Locate every leukocyte (white blood cell).
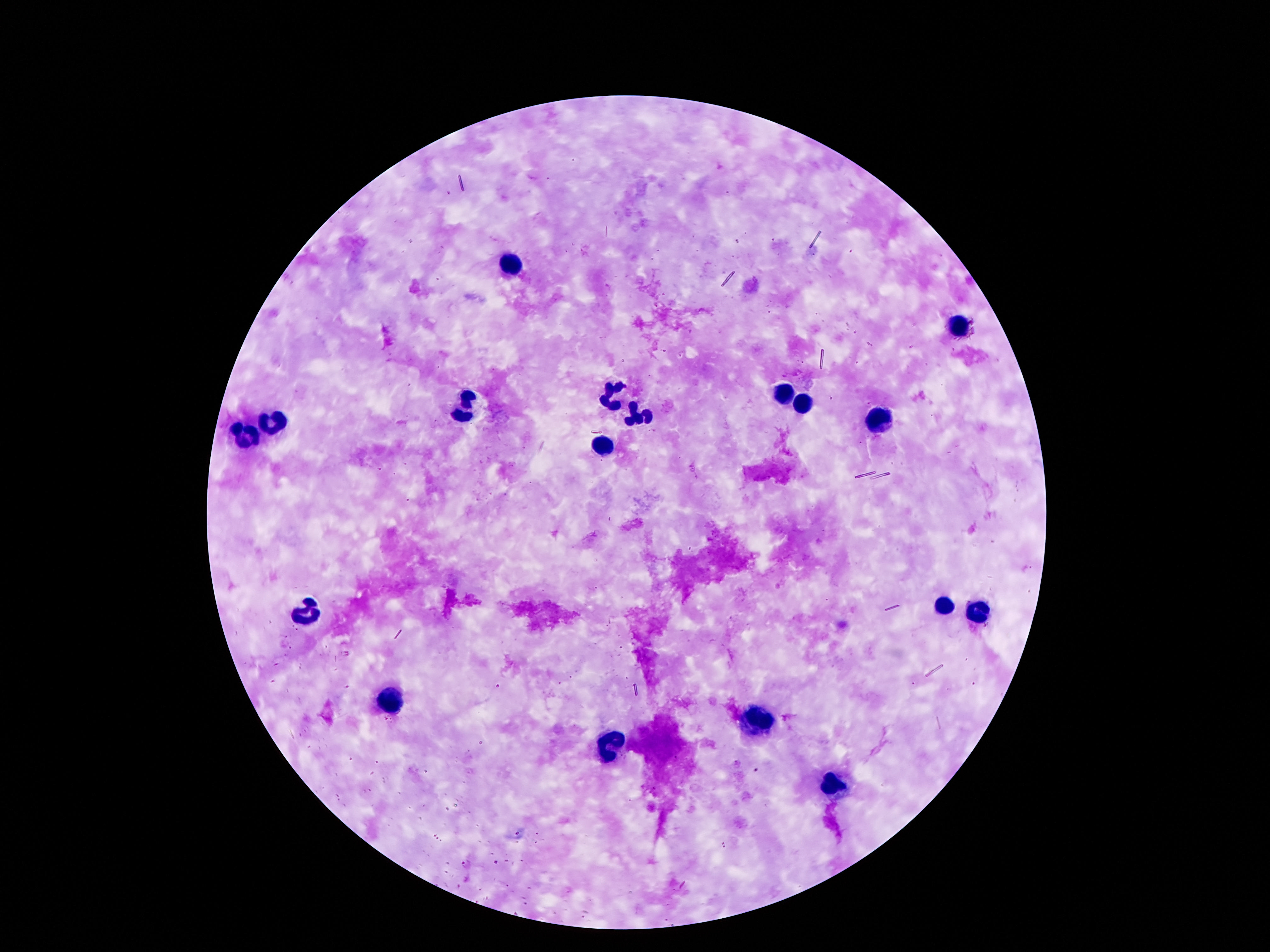
Approximate centers as (x, y) in pixels.
Leukocytes: (511, 264), (955, 329), (616, 396), (782, 400), (465, 405), (801, 410), (640, 414), (273, 420), (880, 422), (244, 431), (607, 446), (945, 606), (304, 611), (974, 614), (393, 701), (758, 719), (614, 746), (835, 780).

image size = 1270×952 pixels
field of view = single
capture = smartphone camera through the microscope eyepiece
patient malaria status = not infected
magnification = 100x
stain = Giemsa
preparation = thick peripheral-blood smear